Give the position of every Plasmodium parasite visible.
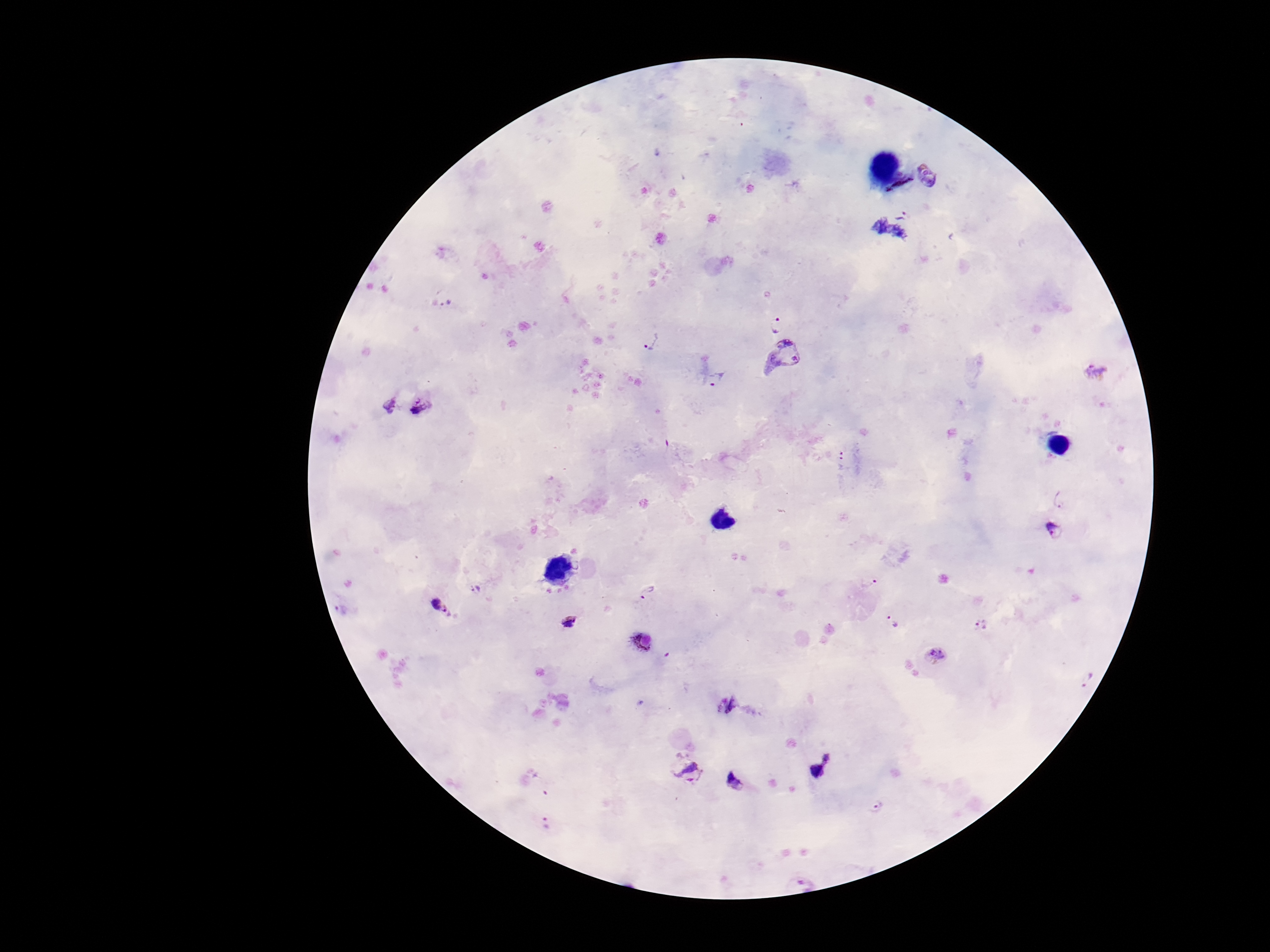

Approximate centers as [x, y] in pixels.
Plasmodium parasites: [929, 175], [901, 214], [445, 298], [778, 318], [650, 342], [786, 360], [1095, 371], [717, 380], [403, 400], [1059, 498], [1053, 529], [868, 581], [476, 589], [646, 590], [439, 605], [342, 609], [892, 620], [568, 623], [981, 625], [643, 641], [936, 654], [727, 703], [821, 762], [688, 770], [736, 782], [877, 806], [547, 823].

Single field of view. Giemsa-stained preparation. Image is 1270×952 pixels. Thick blood smear. Patient malaria status: infected. Smartphone photograph taken through the microscope eyepiece. 100x magnification.